Locate and identify every blood parasite.
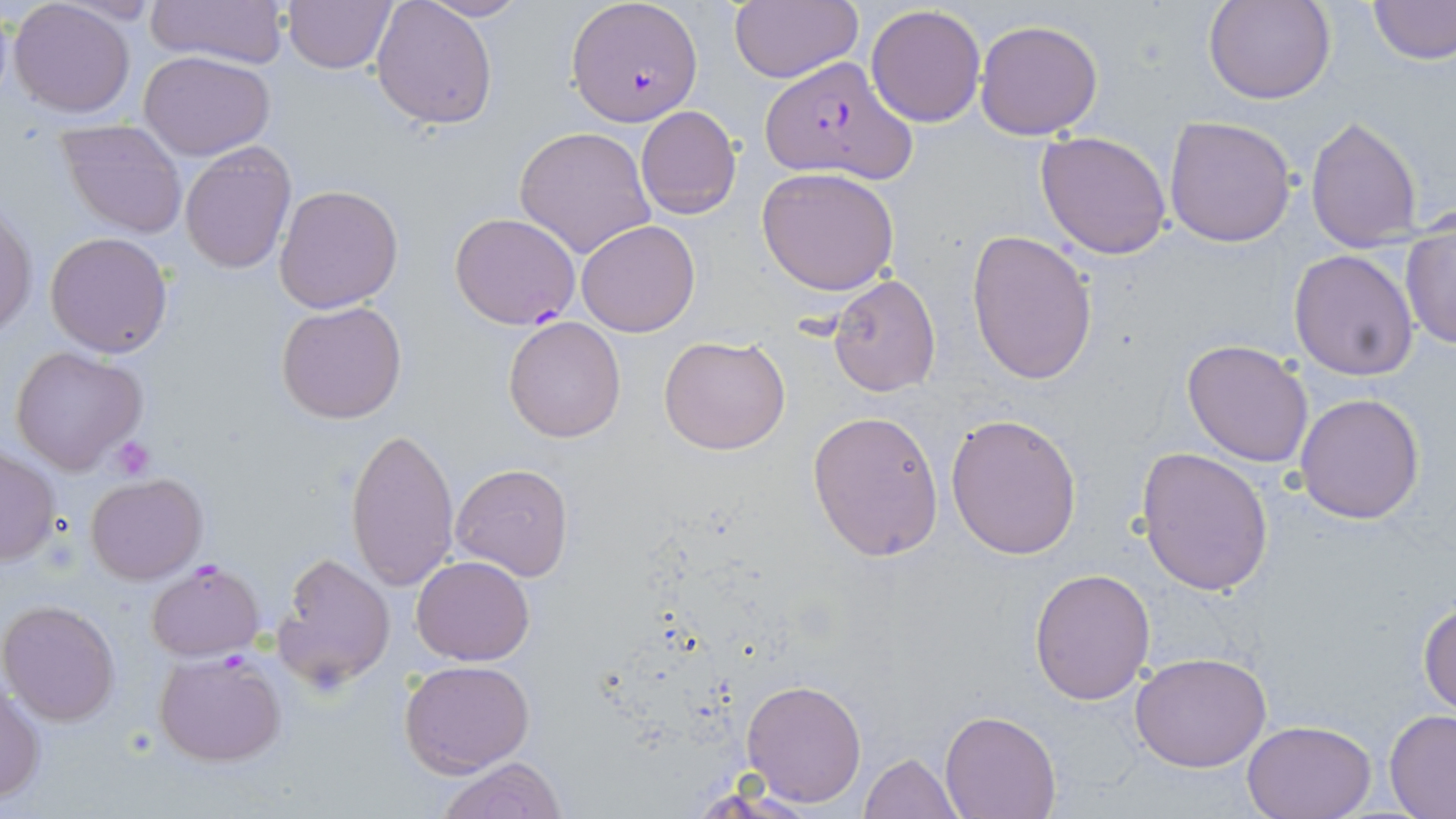
Approximate bounding boxes as named x1/y1/x2/y2 corners in pixels.
Plasmodium falciparum-infected red blood cells: (x1=567, y1=0, x2=702, y2=125), (x1=761, y1=56, x2=915, y2=182), (x1=449, y1=211, x2=581, y2=330), (x1=145, y1=560, x2=264, y2=660), (x1=154, y1=649, x2=288, y2=767).
No Plasmodium ovale, Plasmodium malariae, Plasmodium vivax, Babesia divergens, or Trypanosoma brucei observed.

Summary:
  - Uninfected red blood cell locations: (x1=143, y1=0, x2=289, y2=67), (x1=727, y1=0, x2=862, y2=85), (x1=1205, y1=0, x2=1334, y2=105), (x1=7, y1=1, x2=137, y2=117), (x1=283, y1=1, x2=397, y2=74), (x1=370, y1=1, x2=498, y2=130), (x1=419, y1=1, x2=529, y2=21), (x1=1369, y1=1, x2=1456, y2=66), (x1=866, y1=4, x2=987, y2=128), (x1=975, y1=19, x2=1103, y2=138), (x1=137, y1=50, x2=276, y2=160), (x1=635, y1=106, x2=743, y2=220), (x1=1305, y1=113, x2=1424, y2=253), (x1=1163, y1=114, x2=1298, y2=249), (x1=57, y1=119, x2=188, y2=238), (x1=514, y1=126, x2=656, y2=259), (x1=1035, y1=130, x2=1173, y2=260), (x1=179, y1=143, x2=296, y2=273), (x1=756, y1=166, x2=901, y2=297), (x1=274, y1=184, x2=404, y2=313), (x1=0, y1=205, x2=36, y2=339), (x1=1400, y1=217, x2=1455, y2=350), (x1=575, y1=219, x2=700, y2=337), (x1=966, y1=230, x2=1097, y2=384), (x1=44, y1=231, x2=175, y2=358), (x1=1289, y1=249, x2=1418, y2=379), (x1=829, y1=274, x2=941, y2=397), (x1=277, y1=300, x2=407, y2=424), (x1=502, y1=315, x2=627, y2=443), (x1=659, y1=333, x2=791, y2=456), (x1=1181, y1=339, x2=1314, y2=467), (x1=8, y1=346, x2=150, y2=476), (x1=1294, y1=392, x2=1425, y2=523), (x1=806, y1=410, x2=944, y2=561), (x1=945, y1=413, x2=1082, y2=559), (x1=346, y1=425, x2=459, y2=595), (x1=1, y1=447, x2=60, y2=566), (x1=1137, y1=447, x2=1274, y2=596), (x1=451, y1=462, x2=574, y2=581), (x1=84, y1=474, x2=208, y2=586), (x1=273, y1=551, x2=397, y2=693), (x1=411, y1=555, x2=533, y2=666), (x1=1028, y1=566, x2=1155, y2=705), (x1=1419, y1=596, x2=1456, y2=717), (x1=3, y1=600, x2=121, y2=724), (x1=1131, y1=651, x2=1273, y2=773), (x1=400, y1=659, x2=535, y2=776), (x1=741, y1=677, x2=867, y2=808), (x1=0, y1=684, x2=45, y2=803), (x1=1384, y1=710, x2=1456, y2=817), (x1=940, y1=711, x2=1061, y2=819), (x1=1242, y1=719, x2=1377, y2=819), (x1=860, y1=753, x2=961, y2=818), (x1=436, y1=756, x2=566, y2=818)
  - Platelet locations: (x1=110, y1=435, x2=157, y2=479)
  - Slide-level diagnosis: Plasmodium falciparum
  - Magnification: 1000x
  - Field of view: single
  - Modality: light microscopy
  - Preparation: thin blood film
  - Stain: May-Grünwald-Giemsa
  - Image size: 1456×819 pixels